Mark where platelets are.
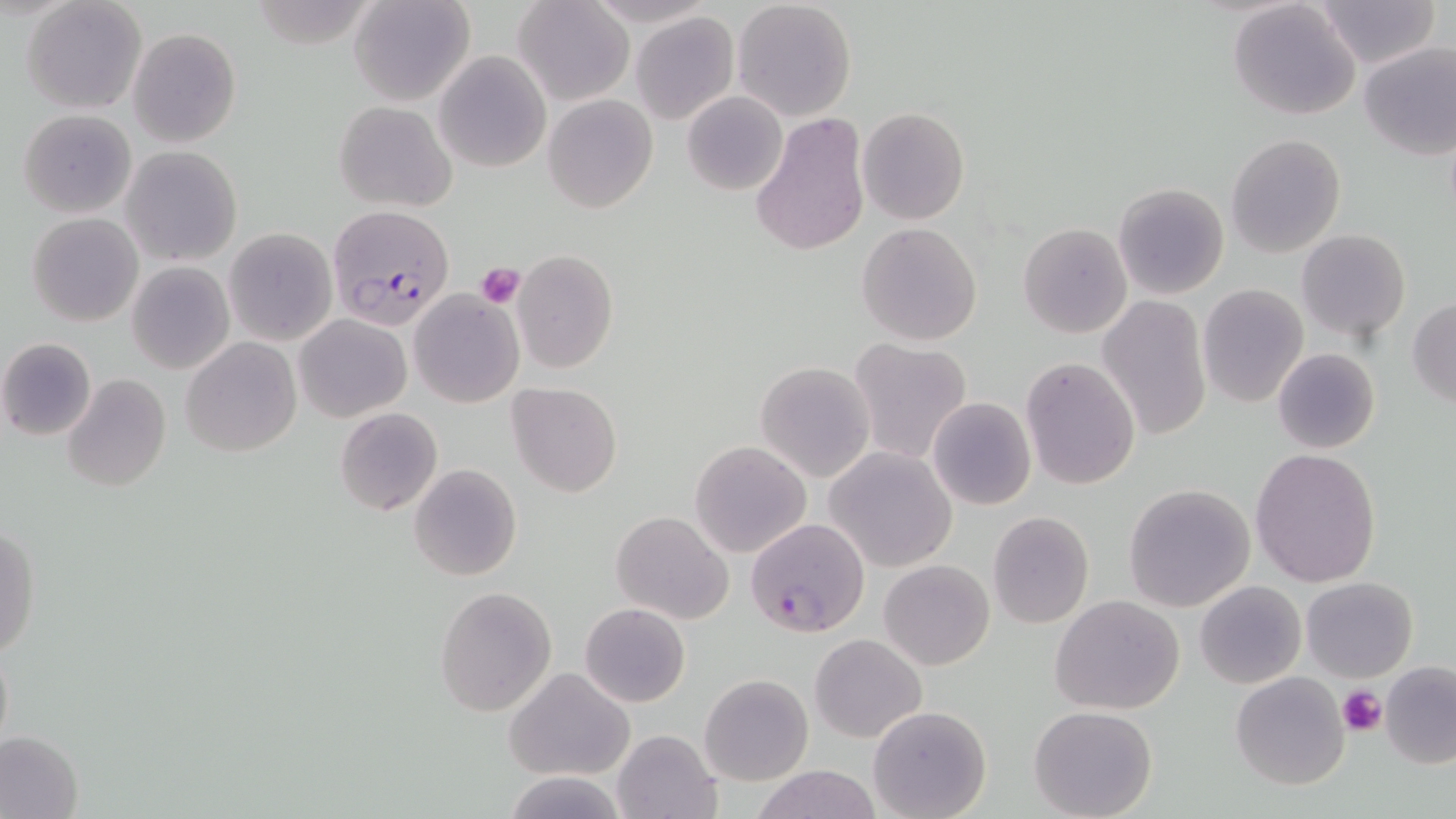

Approximate bounding boxes as (x1, y1, x2, y2) in pixels.
Platelets: (474, 263, 525, 309), (1338, 684, 1386, 738).

Plasmodium falciparum-infected red blood cell locations = approximate bounding boxes as (x1, y1, x2, y2) in pixels: (326, 206, 454, 327), (745, 518, 870, 637)
slide-level diagnosis = Plasmodium falciparum
modality = optical microscopy
preparation = thin blood smear
stain = May-Grünwald-Giemsa
field of view = single
magnification = 1000x
uninfected red blood cell locations = approximate bounding boxes as (x1, y1, x2, y2) in pixels: (22, 0, 146, 114), (348, 0, 475, 108), (1311, 0, 1440, 70), (514, 1, 634, 108), (731, 1, 858, 120), (1230, 1, 1361, 121), (631, 12, 739, 124), (128, 27, 242, 148), (1358, 40, 1456, 160), (434, 51, 551, 172), (682, 91, 787, 195), (543, 95, 657, 212), (334, 100, 456, 211), (858, 107, 969, 226), (18, 108, 137, 219), (750, 111, 871, 258), (1226, 133, 1346, 256), (121, 147, 242, 266), (1113, 181, 1229, 301), (28, 212, 142, 326), (856, 222, 982, 347), (1018, 222, 1132, 338), (224, 228, 336, 344), (1297, 229, 1410, 342), (512, 250, 620, 374), (126, 261, 234, 375), (1196, 284, 1308, 406), (409, 291, 523, 407), (1097, 293, 1213, 442), (1408, 297, 1456, 409), (295, 315, 411, 422), (0, 336, 97, 441), (181, 338, 300, 457), (848, 338, 973, 465), (1272, 348, 1380, 454), (1020, 357, 1140, 489), (755, 360, 875, 482), (62, 373, 172, 493), (507, 383, 624, 498), (927, 396, 1036, 511), (334, 407, 443, 516), (689, 439, 812, 559), (826, 446, 956, 571), (1249, 446, 1382, 588), (409, 464, 521, 582), (1122, 484, 1256, 611), (611, 510, 732, 625), (987, 510, 1094, 630), (1, 523, 39, 662), (881, 559, 994, 669), (1301, 576, 1417, 681), (1195, 581, 1305, 689), (434, 586, 556, 718), (1050, 595, 1186, 714), (579, 603, 690, 708), (809, 633, 925, 743), (1380, 662, 1456, 768), (505, 666, 636, 780), (1230, 673, 1349, 789), (699, 674, 813, 786), (868, 705, 991, 819), (1029, 706, 1159, 819), (0, 727, 84, 819), (611, 729, 723, 819), (751, 764, 882, 819), (505, 772, 629, 817)
image size = 1456×819 pixels